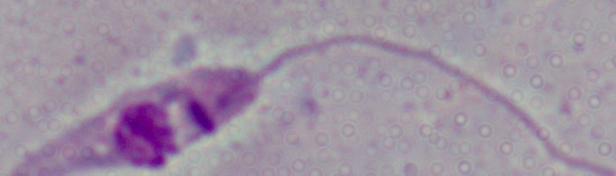

Summary:
  - Identification: Leishmania
  - Modality: micrograph
  - Magnification: 1000x